Locate every Babesia divergens-infected red blood cell.
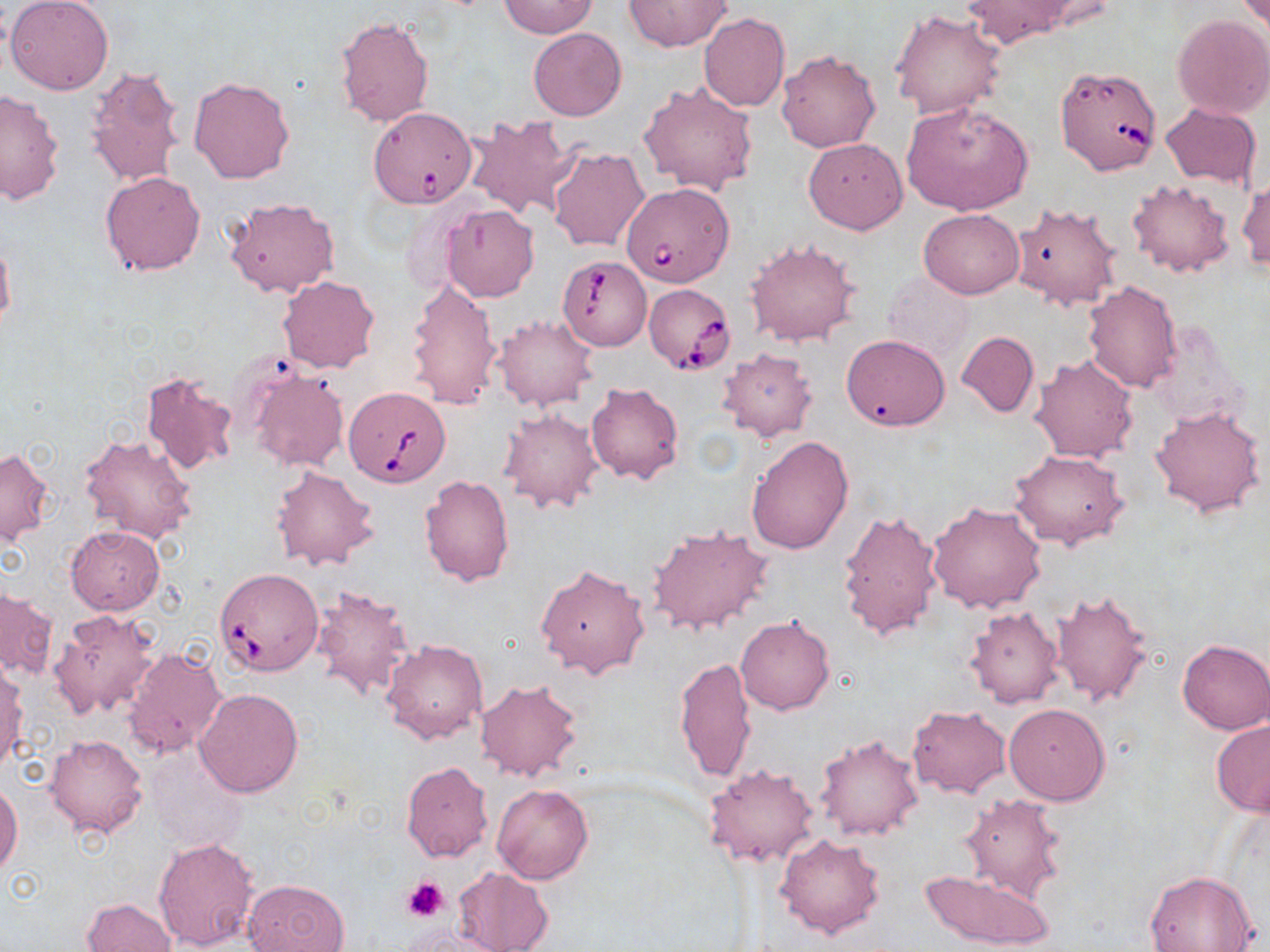
Approximate bounding boxes as (x1, y1, x2, y2) in pixels.
Babesia divergens-infected red blood cells: (1054, 63, 1163, 177), (362, 106, 477, 210), (622, 181, 734, 287), (552, 253, 651, 357), (642, 282, 736, 376), (344, 386, 450, 487), (215, 568, 324, 676).

Uninfected red blood cell locations: (6, 0, 113, 94), (962, 0, 1079, 47), (1236, 0, 1268, 33), (497, 1, 600, 40), (624, 1, 731, 51), (889, 9, 1007, 120), (1172, 13, 1270, 118), (699, 14, 790, 111), (336, 15, 434, 128), (528, 27, 625, 121), (776, 49, 881, 153), (83, 64, 188, 188), (189, 76, 294, 183), (639, 80, 759, 197), (0, 88, 66, 207), (901, 101, 1033, 216), (1160, 103, 1262, 190), (464, 114, 576, 219), (803, 138, 907, 234), (547, 146, 650, 253), (101, 171, 206, 276), (1127, 178, 1236, 278), (1237, 180, 1269, 272), (224, 197, 338, 298), (1012, 202, 1123, 310), (440, 204, 539, 301), (918, 208, 1024, 299), (0, 235, 15, 330), (746, 238, 860, 348), (882, 272, 973, 360), (278, 276, 379, 372), (405, 276, 502, 411), (1083, 281, 1183, 394), (493, 314, 597, 410), (956, 331, 1038, 418), (842, 334, 950, 432), (718, 347, 817, 441), (1030, 352, 1140, 462), (247, 368, 349, 472), (139, 369, 238, 475), (586, 382, 683, 485), (1151, 404, 1265, 519), (497, 407, 603, 513), (80, 433, 197, 544), (747, 436, 854, 556), (1, 447, 53, 546), (1009, 450, 1130, 550), (272, 464, 380, 573), (420, 474, 514, 587), (928, 501, 1046, 613), (836, 508, 944, 643), (648, 524, 775, 637), (65, 526, 165, 615), (534, 563, 650, 680), (310, 584, 416, 702), (1, 587, 56, 681), (1050, 589, 1154, 706), (965, 606, 1063, 709), (48, 609, 159, 719), (735, 616, 833, 715), (1177, 638, 1270, 734), (383, 639, 489, 745), (121, 646, 228, 762), (675, 657, 758, 785), (0, 663, 27, 773), (475, 679, 585, 782), (194, 688, 304, 796), (1004, 703, 1110, 805), (907, 704, 1011, 798), (1211, 721, 1270, 816), (44, 733, 149, 839), (815, 733, 922, 841), (145, 751, 246, 853), (401, 761, 493, 862), (703, 763, 820, 871), (0, 782, 21, 880), (491, 783, 594, 885), (961, 793, 1065, 902), (775, 833, 886, 938), (153, 837, 260, 952), (452, 867, 553, 952), (919, 868, 1055, 950), (1143, 871, 1257, 952), (241, 878, 348, 952), (82, 897, 176, 951), (398, 927, 513, 951). Platelet locations: (400, 875, 451, 923). Slide-level diagnosis: Babesia divergens. One field of a larger specimen. Thin blood smear. May-Grünwald-Giemsa stain. 1000x magnification. Light microscopy. Image is 1270×952 pixels.